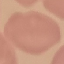

{
  "malaria_status": "uninfected",
  "image_type": "cell patch, automatically extracted from a larger field of view and resized to 64 × 64 pixels",
  "capture": "smartphone through the microscope eyepiece",
  "stain": "Giemsa",
  "preparation": "thin blood smear"
}